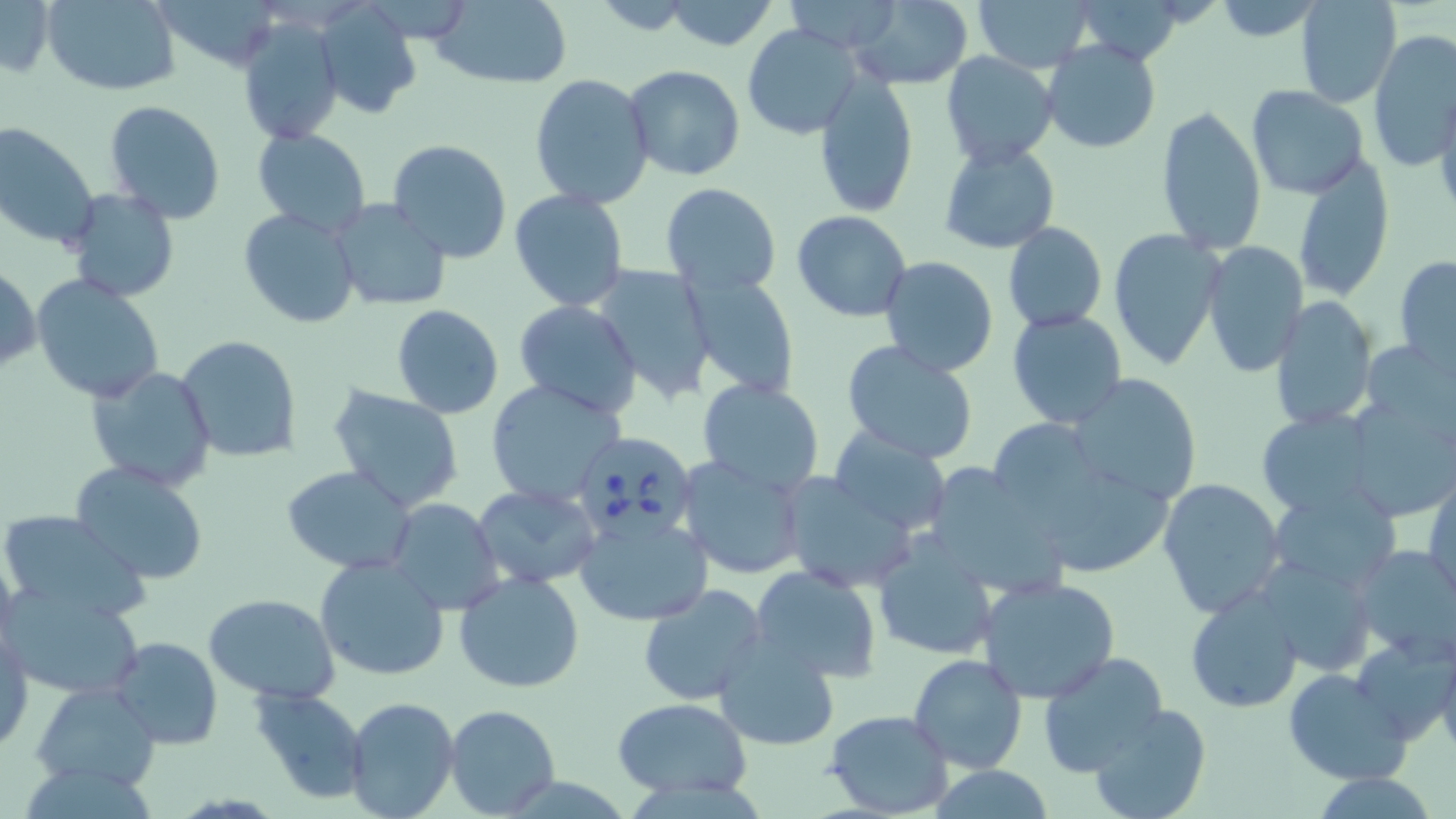
Summary:
  - Coordinate format: approximate bounding boxes as (x1, y1, x2, y2) in pixels
  - Uninfected red blood cell locations: (0, 0, 54, 80), (426, 0, 573, 88), (663, 0, 781, 51), (783, 0, 911, 55), (972, 0, 1095, 72), (1069, 0, 1192, 64), (1297, 0, 1402, 109), (44, 1, 179, 97), (1210, 1, 1324, 42), (845, 2, 973, 88), (316, 3, 422, 121), (233, 17, 342, 143), (739, 22, 859, 140), (1368, 29, 1455, 171), (1041, 38, 1163, 153), (941, 52, 1061, 169), (624, 66, 745, 182), (812, 71, 918, 217), (530, 74, 655, 209), (1245, 86, 1368, 198), (1433, 90, 1456, 220), (102, 100, 228, 225), (1156, 105, 1267, 254), (0, 123, 100, 252), (253, 128, 372, 237), (387, 138, 512, 265), (938, 143, 1059, 254), (1290, 153, 1395, 303), (660, 181, 782, 297), (63, 188, 180, 302), (508, 189, 631, 312), (329, 202, 450, 311), (238, 206, 361, 329), (792, 210, 912, 322), (1003, 222, 1107, 332), (1107, 229, 1226, 371), (1202, 241, 1309, 378), (1394, 254, 1456, 373), (879, 256, 1000, 376), (1, 264, 39, 374), (588, 264, 717, 402), (685, 273, 800, 400), (32, 275, 166, 406), (1268, 296, 1375, 431), (513, 301, 642, 416), (392, 304, 504, 418), (1007, 309, 1127, 428), (176, 336, 303, 464), (1358, 337, 1456, 449), (840, 339, 982, 463), (87, 364, 217, 491), (1066, 373, 1203, 506), (485, 379, 628, 509), (697, 379, 825, 494), (327, 383, 466, 513), (1340, 398, 1456, 520), (1255, 409, 1385, 520), (826, 429, 952, 534), (677, 452, 810, 581), (68, 461, 210, 584), (282, 465, 417, 573), (922, 465, 1070, 597), (1426, 469, 1456, 608), (779, 472, 918, 594), (1158, 478, 1288, 620), (472, 484, 601, 587), (1266, 484, 1401, 596), (386, 498, 504, 616), (1, 510, 151, 624), (576, 513, 713, 627), (872, 532, 998, 661), (1349, 543, 1456, 662), (315, 553, 452, 681), (1252, 553, 1378, 679), (748, 566, 883, 682), (453, 572, 586, 694), (975, 575, 1122, 705), (5, 581, 142, 701), (639, 584, 769, 703), (1186, 588, 1305, 713), (205, 593, 340, 704), (1, 629, 32, 752), (713, 633, 840, 750), (1437, 635, 1456, 761), (108, 637, 225, 750), (1351, 637, 1456, 744), (1037, 651, 1169, 778), (909, 653, 1029, 776), (1285, 668, 1412, 783), (32, 680, 161, 790), (248, 688, 367, 804), (341, 696, 460, 819), (612, 697, 752, 799), (1085, 703, 1211, 819), (445, 704, 561, 817), (824, 710, 952, 817), (926, 764, 1059, 819), (1310, 774, 1441, 819)
  - Babesia divergens-infected red blood cell locations: (580, 435, 694, 548)
  - Slide-level diagnosis: Babesia divergens
  - Field of view: one of a larger specimen
  - Magnification: 1000x
  - Preparation: thin blood film
  - Image size: 1456×819 pixels
  - Modality: light microscopy
  - Stain: May-Grünwald-Giemsa